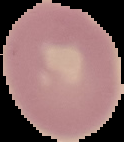 Image is 124×142 pixels. Result: negative for malaria parasites. From a thin blood smear. The area outside the segmented cell region is set to black.